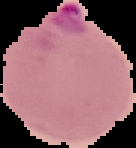 Image is 136×148 pixels. Malaria status: parasitized. Cell region segmented out of the field of view; the surrounding area is masked to black. From a thin blood smear.